Classify this cell by malaria status.
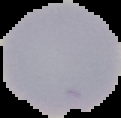

It is uninfected.

From a thin blood smear. The area outside the segmented cell region is set to black. Image is 121×118 pixels.